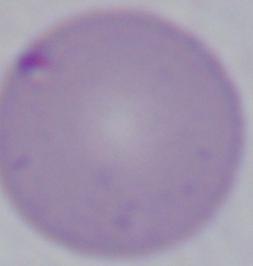
{
  "modality": "photomicrograph",
  "identification": "Babesia",
  "magnification": "1000x"
}